Give the position of every Plasmodium parasite visible.
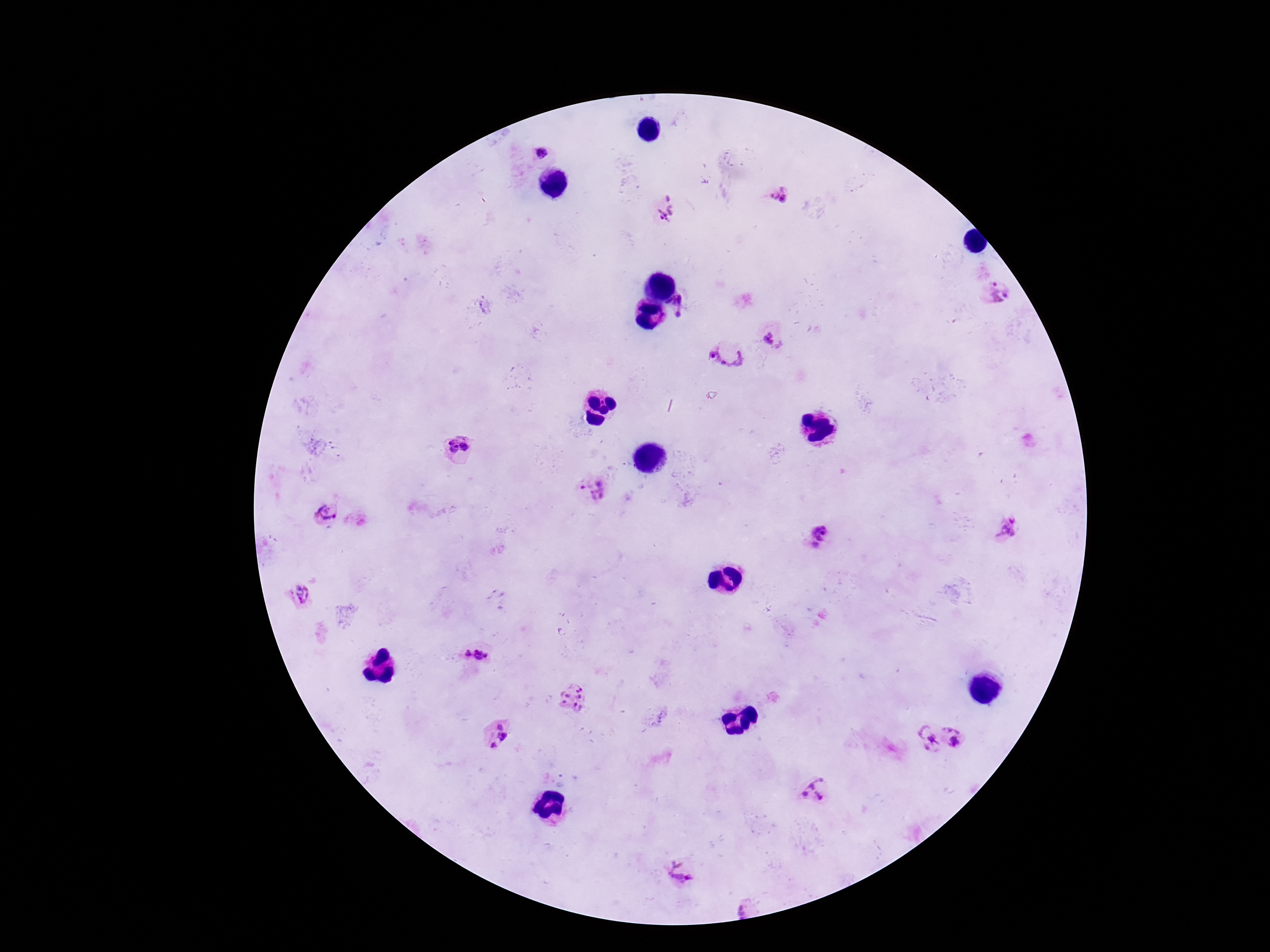

Approximate object centers, in pixels from the top-left corner.
Plasmodium parasites: (x=541, y=154), (x=778, y=195), (x=667, y=208), (x=994, y=293), (x=678, y=308), (x=769, y=337), (x=727, y=351), (x=457, y=448), (x=590, y=490), (x=329, y=514), (x=1008, y=529), (x=820, y=540), (x=300, y=593), (x=466, y=654), (x=482, y=654), (x=573, y=698), (x=500, y=725), (x=954, y=736), (x=502, y=737), (x=926, y=739), (x=493, y=745), (x=813, y=790), (x=682, y=870), (x=742, y=908).

{
  "stain": "Giemsa",
  "capture": "smartphone camera through the microscope eyepiece",
  "preparation": "thick peripheral-blood smear",
  "image_size": "1270×952 pixels",
  "magnification": "100x",
  "field_of_view": "single",
  "patient_malaria_status": "infected"
}